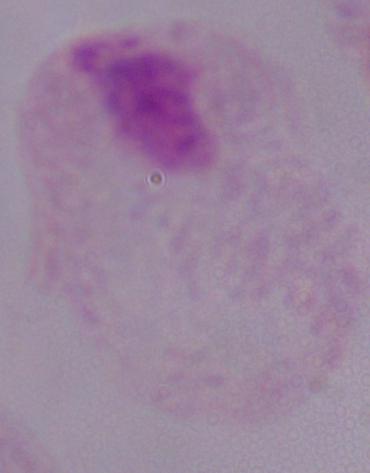

1000x magnification. A trichomonad is shown. Photomicrograph.